Locate every Plasmodium parasite.
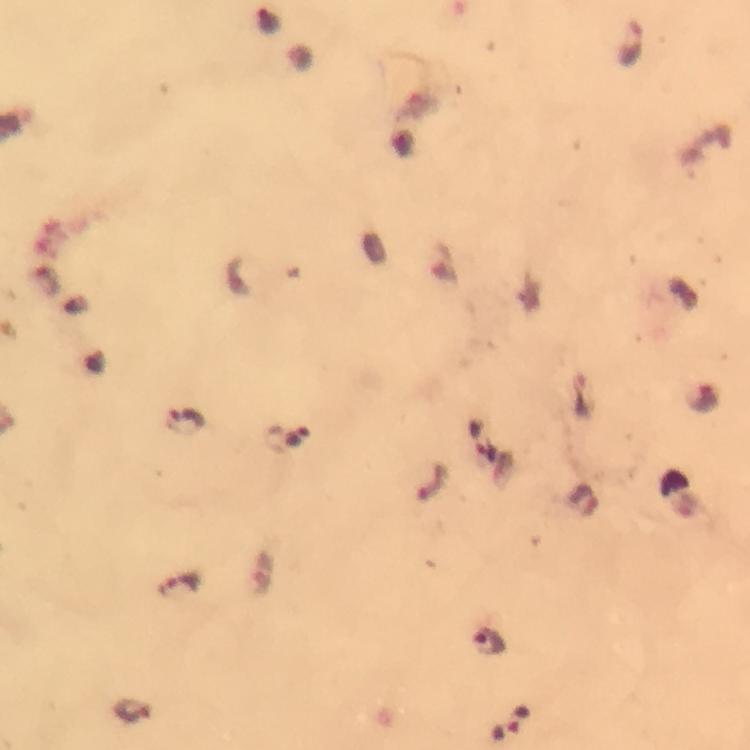
Approximate centers as {x, y} in pixels.
Plasmodium parasites: {632, 45}, {701, 398}, {185, 422}, {179, 585}, {490, 641}, {132, 710}.

stain = Giemsa
magnification = 100x
image size = 750×750 pixels
preparation = thick blood smear
cropped from = one field of view
immersion oil = applied
context = from a diagnostic examination for malaria
capture = smartphone photograph through a microscope